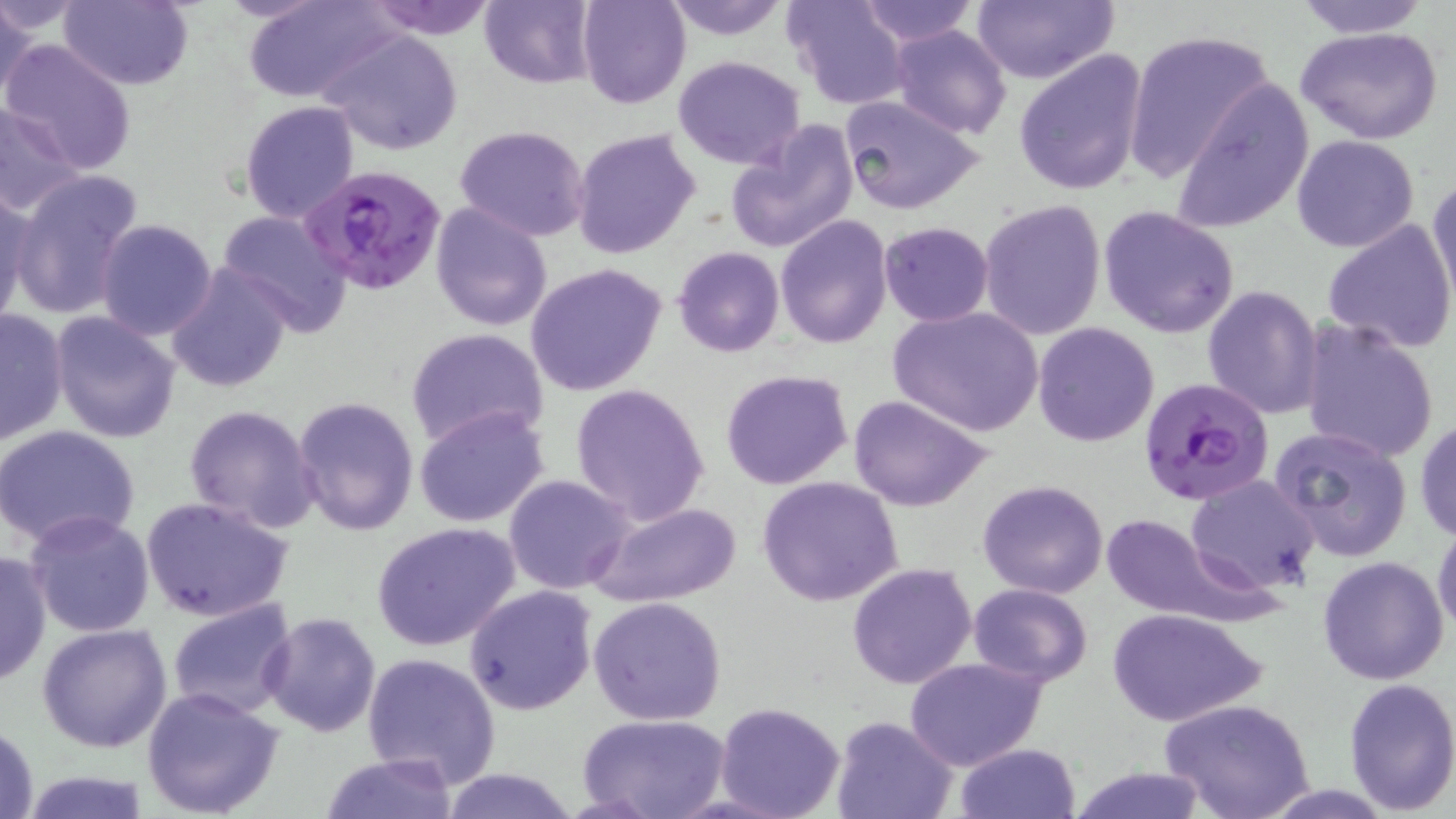
slide_level_diagnosis: Plasmodium falciparum
stain: May-Grünwald-Giemsa
preparation: thin blood film
uninfected_red_blood_cell_locations: 'approximate bounding boxes as (x1, y1, x2, y2) in pixels: (58, 0, 194, 89), (241, 0, 397, 103), (362, 0, 498, 38), (480, 0, 598, 88), (576, 0, 690, 109), (660, 0, 792, 42), (785, 0, 911, 110), (971, 0, 1120, 86), (1293, 0, 1433, 39), (1, 1, 40, 107), (855, 1, 980, 47), (888, 23, 1011, 139), (1295, 24, 1445, 146), (1122, 28, 1275, 181), (323, 30, 463, 155), (3, 40, 139, 175), (1014, 47, 1149, 196), (672, 56, 805, 169), (1172, 80, 1315, 232), (837, 92, 987, 216), (239, 100, 359, 223), (0, 101, 84, 217), (724, 123, 859, 255), (455, 126, 591, 242), (572, 127, 701, 258), (1291, 135, 1419, 254), (8, 167, 145, 321), (1428, 175, 1456, 304), (0, 183, 36, 328), (978, 200, 1108, 341), (430, 201, 552, 331), (1097, 205, 1241, 339), (214, 209, 353, 331), (775, 214, 892, 348), (95, 217, 218, 339), (1323, 220, 1455, 354), (878, 221, 994, 327), (672, 247, 783, 357), (525, 262, 667, 397), (165, 263, 295, 393), (1201, 284, 1325, 419), (886, 306, 1044, 437), (0, 308, 69, 448), (50, 309, 182, 446), (1298, 320, 1440, 465), (1032, 321, 1160, 447), (404, 327, 551, 450), (719, 369, 854, 491), (570, 381, 710, 525), (848, 394, 994, 512), (292, 396, 420, 539), (184, 405, 321, 534), (413, 405, 551, 530), (1415, 416, 1456, 543), (1269, 424, 1414, 561), (0, 425, 141, 551), (504, 473, 634, 595), (1186, 474, 1320, 595), (756, 477, 903, 608), (976, 479, 1109, 599), (141, 496, 296, 624), (585, 501, 743, 608), (25, 511, 156, 638), (1100, 511, 1275, 630), (372, 521, 521, 651), (1432, 522, 1456, 636), (0, 551, 51, 689), (1317, 555, 1451, 686), (847, 563, 977, 690), (967, 583, 1093, 687), (464, 585, 598, 716), (588, 595, 728, 726), (165, 598, 297, 721), (1106, 607, 1268, 728), (261, 612, 381, 737), (37, 623, 173, 754), (362, 651, 500, 787), (905, 658, 1046, 770), (1341, 676, 1456, 815), (142, 687, 286, 818), (1161, 698, 1315, 819), (715, 702, 846, 819), (577, 713, 729, 819), (832, 714, 956, 819), (1, 720, 41, 819), (954, 743, 1080, 819), (319, 754, 461, 817), (439, 767, 581, 819), (1063, 767, 1210, 819), (13, 770, 154, 819)'
plasmodium_falciparum_infected_red_blood_cell_locations: 'approximate bounding boxes as (x1, y1, x2, y2) in pixels: (303, 165, 447, 296), (1138, 377, 1275, 505)'
magnification: 1000x
field_of_view: one of a larger specimen
image_size: 1456×819 pixels
modality: light microscopy